Outline each blood parasite and name the species.
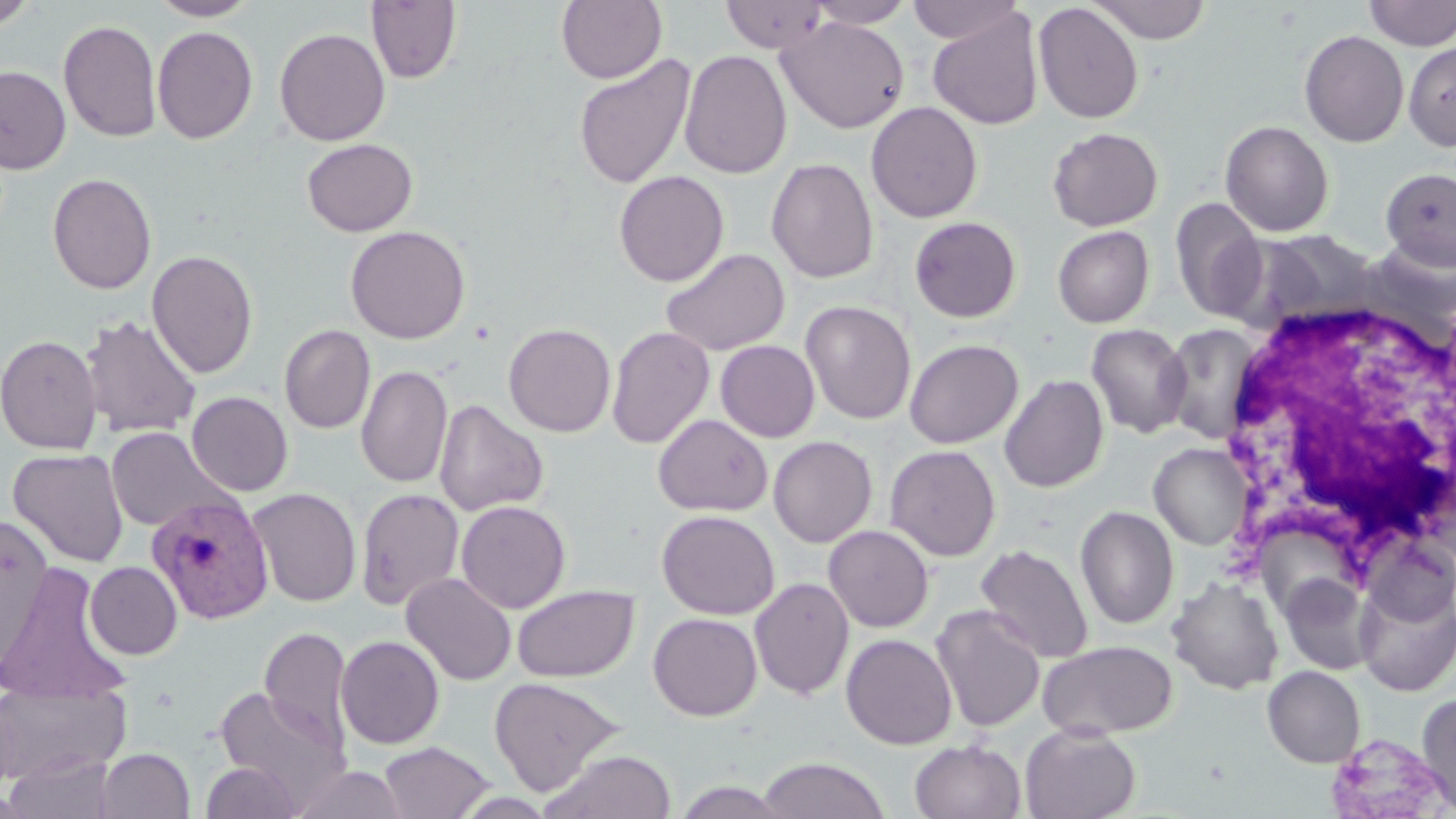

Approximate bounding boxes as (x1,y1)-(x2,y2) corner pairs in pixels.
Plasmodium vivax-infected red blood cells: (147,492)-(274,625), (1322,732)-(1455,819).
No Plasmodium falciparum, Plasmodium ovale, Plasmodium malariae, Babesia divergens, or Trypanosoma brucei observed.

Summary:
  - Uninfected red blood cell locations: (0,0)-(38,31), (149,0)-(260,20), (556,0)-(668,84), (805,0)-(916,28), (906,0)-(1023,45), (1088,0)-(1212,44), (1364,0)-(1456,51), (366,1)-(461,84), (721,1)-(830,54), (1033,2)-(1144,124), (927,8)-(1044,130), (776,16)-(910,134), (58,20)-(162,143), (152,26)-(257,145), (274,27)-(390,146), (1299,30)-(1409,147), (1403,42)-(1456,152), (679,49)-(792,179), (573,53)-(696,191), (1,65)-(71,174), (866,101)-(983,223), (1220,120)-(1334,237), (1048,127)-(1163,231), (301,138)-(417,237), (766,158)-(879,284), (1381,167)-(1456,268), (614,170)-(729,286), (47,173)-(157,294), (1169,197)-(1268,323), (909,216)-(1022,323), (345,225)-(471,344), (1052,225)-(1154,328), (1253,229)-(1381,326), (661,248)-(790,356), (147,249)-(259,379), (800,300)-(917,425), (80,315)-(201,439), (503,323)-(616,437), (1086,323)-(1192,439), (1160,323)-(1265,444), (279,324)-(376,434), (606,325)-(715,448), (0,334)-(103,455), (904,339)-(1023,449), (715,340)-(820,442), (356,364)-(453,488), (999,375)-(1109,493), (186,391)-(293,496), (434,399)-(548,518), (653,414)-(772,517), (105,426)-(233,532), (768,436)-(877,547), (1149,442)-(1252,550), (885,445)-(1001,561), (8,448)-(129,567), (248,488)-(361,607), (356,488)-(464,610), (456,500)-(571,613), (1075,506)-(1179,628), (656,509)-(780,620), (0,515)-(54,666), (823,525)-(934,632), (1362,536)-(1456,629), (975,544)-(1094,664), (0,562)-(132,704), (85,562)-(182,659), (401,572)-(516,686), (1281,575)-(1377,675), (749,577)-(854,699), (1167,577)-(1285,695), (512,585)-(638,682), (1355,585)-(1456,696), (931,605)-(1046,733), (648,613)-(762,721), (259,627)-(352,750), (840,633)-(957,750), (335,635)-(444,749), (1038,640)-(1178,739), (1262,665)-(1365,768), (489,676)-(625,797), (0,682)-(131,786), (214,686)-(348,806), (0,689)-(19,802), (1416,691)-(1456,814), (1019,723)-(1141,819), (910,740)-(1026,819), (378,741)-(496,819), (95,748)-(194,819), (542,749)-(677,818), (4,754)-(118,818), (757,756)-(889,819), (200,760)-(302,819), (289,764)-(408,819)
  - White blood cell locations: (1220,292)-(1456,567)
  - Slide-level diagnosis: Plasmodium vivax
  - Modality: optical microscopy
  - Preparation: thin blood smear
  - Image size: 1456×819 pixels
  - Field of view: one of a larger specimen
  - Stain: May-Grünwald-Giemsa
  - Magnification: 1000x